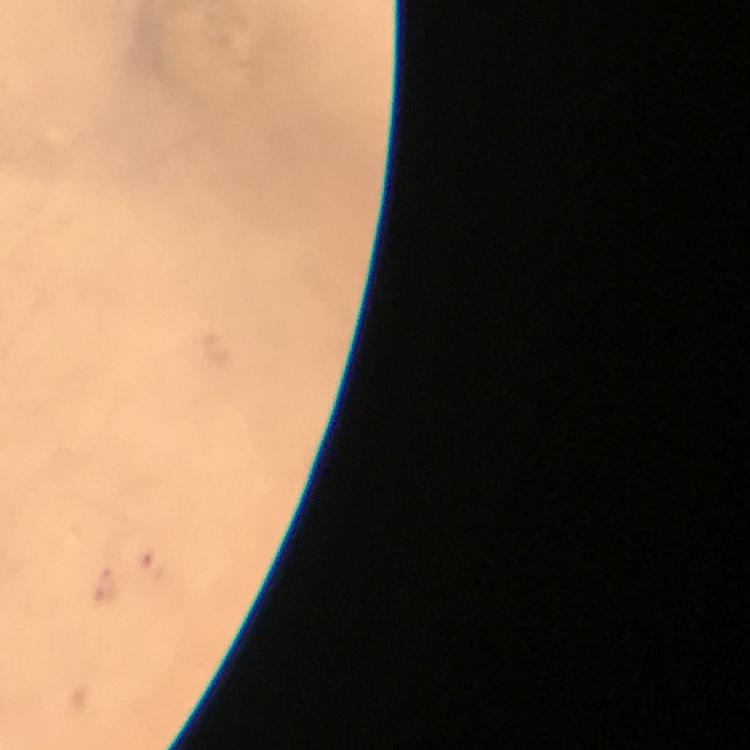 Approximate centers as {x, y} in pixels. Plasmodium parasite locations: {152, 563}. A crop from one field of view. Giemsa stain. Immersion oil applied. Image is 750×750 pixels. Thick blood smear. Photographed through the microscope with a smartphone camera. At 100x magnification. From a diagnostic examination for malaria.